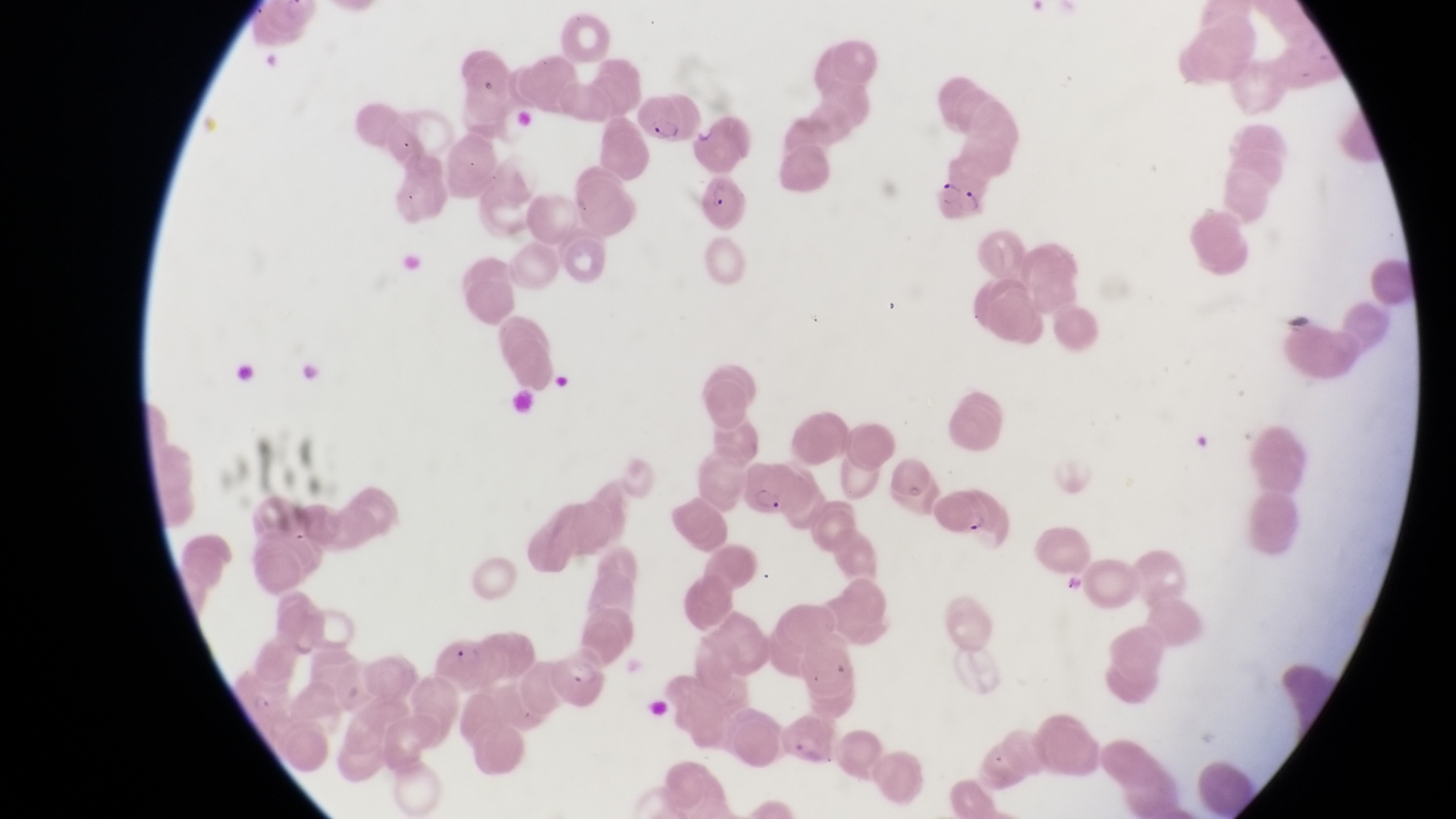

Approximate bounding boxes as (left, top, right, bottom) in pixels.
Summary:
  - Parasitised red blood cell locations: (637, 87, 689, 146), (933, 162, 992, 221), (703, 175, 748, 227), (748, 465, 807, 524), (930, 485, 994, 541), (435, 631, 495, 691), (552, 639, 611, 716)
  - Artifact (platelet-like body, stain precipitate, or debris) locations: (1284, 307, 1313, 341)
  - Country: Uganda
  - Image size: 1456×819 pixels
  - Magnification: 1000x
  - Capture: smartphone photograph through the eyepiece of an Olympus CX-23 microscope
  - Field of view: single
  - Preparation: thin blood smear